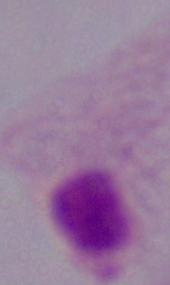

A trichomonad is seen. 1000x magnification. Photomicrograph.